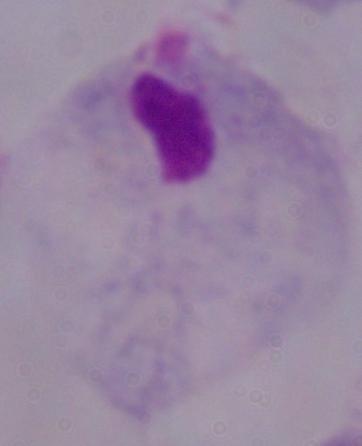

modality = photomicrograph
magnification = 1000x
identification = trichomonad